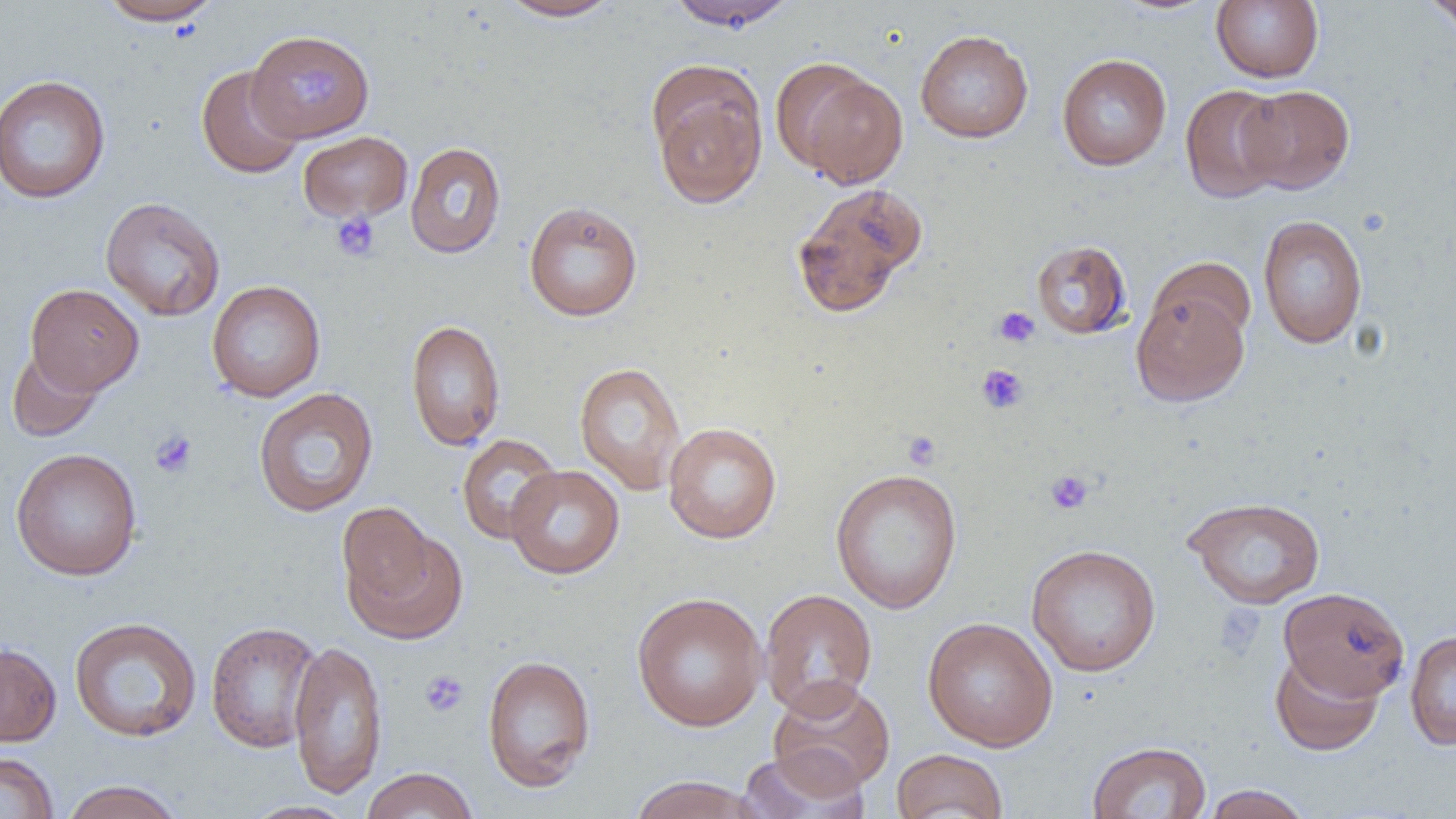

slide-level diagnosis = no evidence of blood parasites
image size = 1456×819 pixels
magnification = 1000x
modality = light microscopy
uninfected red blood cell locations = approximate bounding boxes as (x1, y1, x2, y2) in pixels: (98, 0, 222, 26), (498, 0, 624, 21), (664, 0, 798, 31), (1211, 0, 1324, 83), (1421, 0, 1456, 34), (915, 29, 1034, 143), (246, 30, 374, 141), (1057, 53, 1172, 170), (776, 61, 908, 188), (196, 65, 305, 179), (647, 65, 768, 209), (0, 74, 111, 204), (1179, 84, 1288, 204), (1238, 85, 1354, 194), (297, 130, 413, 223), (405, 142, 506, 258), (791, 182, 927, 317), (100, 196, 225, 321), (524, 201, 643, 322), (1258, 214, 1368, 348), (1031, 239, 1132, 339), (1148, 256, 1256, 348), (206, 280, 326, 402), (25, 283, 144, 395), (1131, 286, 1250, 407), (406, 319, 506, 451), (7, 346, 104, 443), (574, 361, 687, 495), (253, 387, 379, 517), (662, 422, 782, 544), (456, 434, 562, 544), (10, 447, 143, 580), (505, 464, 624, 579), (829, 467, 963, 614), (1184, 495, 1326, 609), (342, 513, 466, 645), (1026, 543, 1162, 676), (1278, 587, 1410, 701), (758, 588, 878, 719), (631, 591, 767, 732), (69, 616, 202, 742), (922, 617, 1058, 752), (205, 621, 322, 753), (1405, 629, 1456, 751), (288, 638, 388, 798), (0, 641, 62, 747), (1270, 650, 1384, 756), (482, 654, 596, 792), (767, 678, 896, 795), (1087, 741, 1212, 819), (738, 747, 871, 818), (891, 748, 1008, 819), (0, 752, 59, 818), (360, 767, 479, 819), (628, 774, 764, 819), (59, 780, 186, 819), (1201, 784, 1313, 819), (240, 800, 358, 819)
field of view = one of a larger specimen
platelet locations = approximate bounding boxes as (x1, y1, x2, y2) in pixels: (284, 58, 349, 119), (330, 211, 381, 262), (992, 306, 1041, 349), (976, 364, 1028, 414), (149, 429, 198, 479), (901, 430, 942, 470), (1045, 469, 1094, 514), (420, 670, 469, 717)
preparation = thin blood film